Outline each Plasmodium vivax-infected red blood cell.
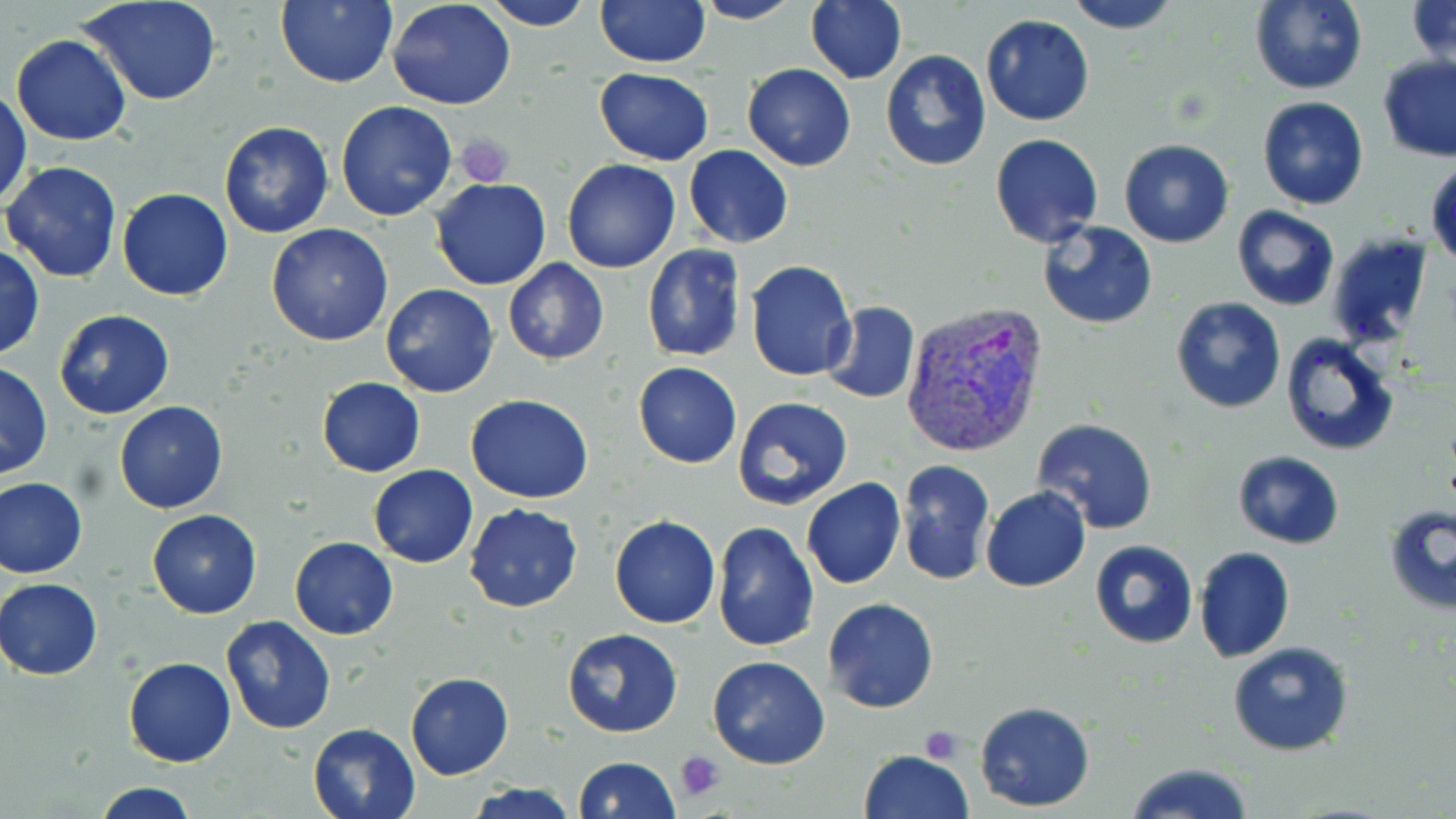

Approximate bounding boxes as (x1, y1, x2, y2) in pixels.
Plasmodium vivax-infected red blood cells: (899, 304, 1050, 461).

Summary:
  - Uninfected red blood cell locations: (276, 0, 398, 88), (483, 0, 597, 30), (594, 0, 709, 68), (1064, 0, 1183, 33), (1249, 0, 1368, 94), (1406, 0, 1455, 70), (80, 1, 223, 107), (388, 1, 516, 111), (691, 1, 803, 24), (805, 1, 907, 83), (981, 13, 1095, 125), (11, 34, 131, 145), (879, 48, 991, 172), (1376, 55, 1456, 162), (741, 63, 856, 170), (593, 68, 715, 165), (1, 87, 31, 209), (1257, 96, 1369, 209), (335, 100, 457, 221), (218, 120, 336, 239), (989, 133, 1104, 248), (1119, 139, 1234, 248), (684, 145, 794, 249), (2, 159, 123, 283), (562, 159, 681, 274), (1428, 160, 1456, 269), (430, 177, 552, 291), (117, 188, 234, 301), (1231, 206, 1340, 311), (1039, 220, 1158, 329), (266, 224, 394, 346), (1326, 231, 1435, 350), (641, 244, 746, 361), (0, 245, 45, 360), (503, 258, 609, 365), (746, 260, 857, 381), (381, 284, 499, 398), (1170, 297, 1287, 416), (821, 301, 922, 405), (53, 309, 175, 420), (1279, 334, 1399, 457), (0, 361, 51, 480), (632, 361, 742, 468), (315, 377, 424, 477), (465, 394, 594, 502), (731, 396, 852, 510), (114, 400, 228, 514), (1033, 419, 1158, 534), (1231, 450, 1346, 548), (896, 460, 993, 585), (368, 466, 478, 568), (1, 475, 88, 578), (801, 477, 906, 590), (982, 486, 1091, 593), (464, 502, 584, 612), (1385, 505, 1456, 615), (147, 509, 262, 619), (609, 516, 720, 629), (714, 520, 820, 652), (289, 537, 398, 639), (1090, 539, 1198, 649), (1193, 547, 1295, 663), (0, 577, 103, 679), (823, 597, 939, 714), (219, 616, 338, 735), (562, 627, 683, 738), (1228, 642, 1353, 756), (706, 656, 831, 769), (123, 658, 235, 767), (404, 672, 514, 780), (975, 700, 1096, 812), (307, 722, 422, 818), (859, 749, 974, 818), (573, 756, 681, 818), (1122, 762, 1254, 819), (88, 781, 204, 818), (463, 783, 581, 818)
  - Platelet locations: (457, 133, 515, 186), (920, 726, 964, 762), (674, 751, 726, 800)
  - Slide-level diagnosis: Plasmodium vivax
  - Stain: May-Grünwald-Giemsa
  - Magnification: 1000x
  - Modality: light microscopy
  - Image size: 1456×819 pixels
  - Preparation: thin blood smear
  - Field of view: single